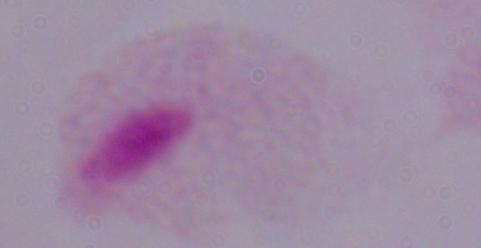

Photomicrograph. A trichomonad is shown. 1000x magnification.